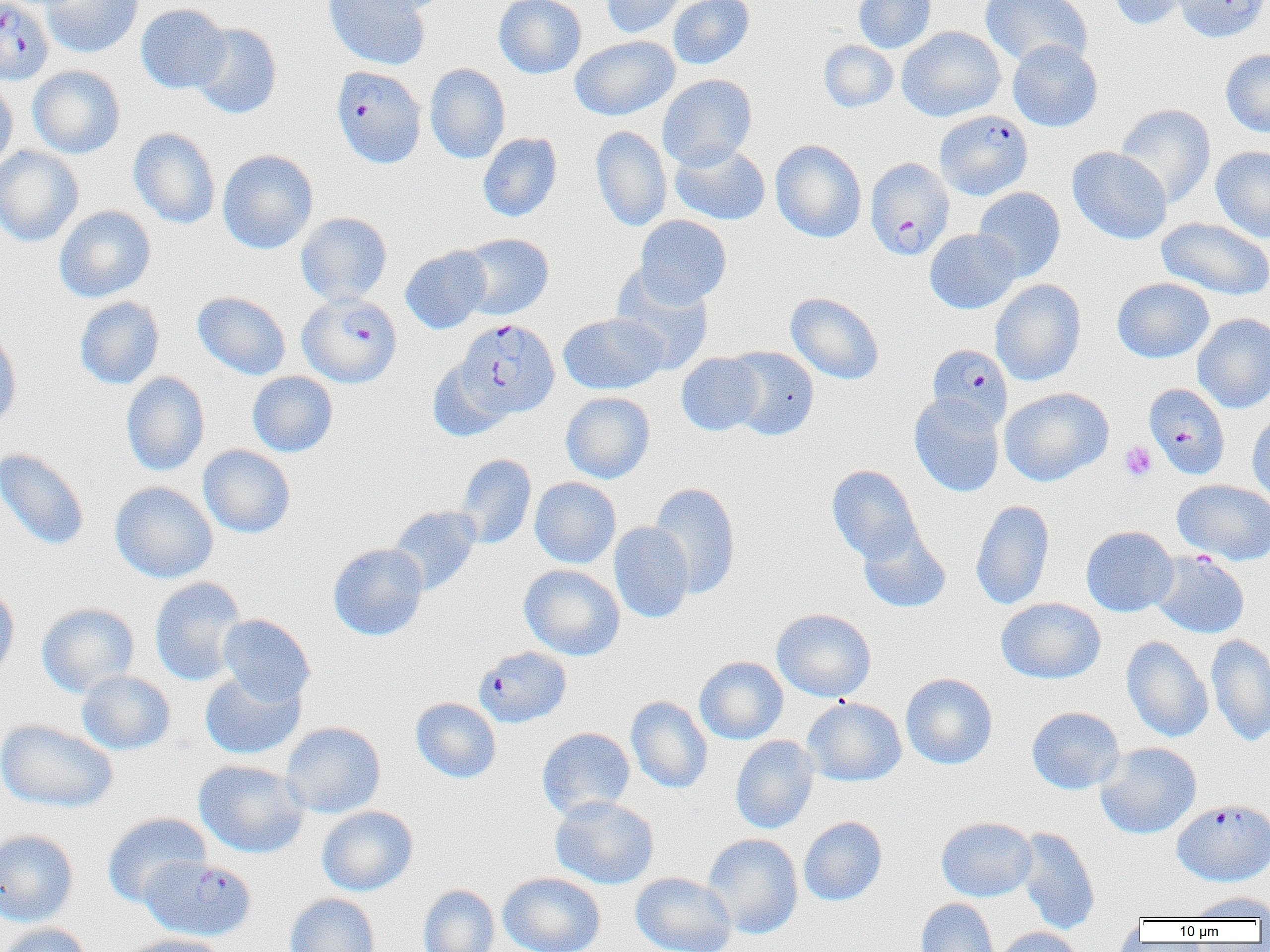
slide-level diagnosis = Plasmodium falciparum
image size = 1270×952 pixels
magnification = 1000x
platelet locations = approximate bounding boxes as [x1, y1, x2, y2] in pixels: [1119, 441, 1158, 481]
field of view = single
modality = light microscopy
Plasmodium falciparum-infected red blood cell locations = approximate bounding boxes as [x1, y1, x2, y2] in pixels: [0, 0, 53, 84], [331, 65, 427, 168], [934, 110, 1033, 200], [868, 157, 957, 259], [297, 293, 402, 387], [455, 318, 560, 419], [927, 343, 1013, 431], [1144, 383, 1230, 479], [474, 646, 572, 727], [1172, 799, 1270, 887], [139, 856, 257, 941]
preparation = thin blood smear
uninfected red blood cell locations = approximate bounding boxes as [x1, y1, x2, y2] in pixels: [41, 0, 143, 58], [323, 0, 431, 70], [354, 0, 453, 15], [493, 0, 586, 79], [600, 0, 689, 38], [668, 0, 754, 69], [853, 0, 936, 53], [979, 0, 1093, 69], [1107, 0, 1195, 30], [1172, 0, 1270, 42], [136, 4, 231, 93], [191, 22, 283, 119], [897, 26, 1006, 122], [570, 35, 679, 120], [818, 40, 898, 112], [1007, 40, 1103, 132], [1220, 49, 1270, 138], [425, 63, 510, 163], [27, 65, 126, 158], [657, 73, 757, 171], [0, 76, 18, 172], [1115, 104, 1216, 208], [590, 126, 672, 231], [128, 128, 221, 229], [478, 132, 562, 222], [770, 140, 867, 242], [670, 142, 771, 225], [1211, 145, 1270, 243], [0, 146, 84, 247], [1067, 146, 1172, 244], [218, 149, 318, 254], [973, 186, 1065, 281], [54, 205, 156, 302], [295, 212, 392, 304], [635, 215, 731, 308], [1156, 217, 1270, 301], [924, 228, 1022, 314], [457, 233, 554, 320], [400, 245, 492, 334], [610, 267, 716, 375], [1112, 277, 1214, 363], [990, 278, 1086, 386], [192, 291, 291, 380], [785, 291, 885, 385], [74, 296, 165, 389], [558, 312, 669, 395], [1192, 313, 1270, 413], [0, 328, 22, 432], [724, 346, 819, 440], [677, 352, 764, 435], [428, 360, 512, 442], [121, 371, 210, 476], [247, 371, 338, 457], [999, 387, 1114, 486], [561, 392, 655, 484], [909, 393, 1004, 496], [1247, 411, 1270, 508], [198, 445, 295, 538], [0, 447, 90, 551], [455, 453, 537, 548], [827, 464, 921, 564], [530, 477, 621, 568], [1173, 479, 1270, 565], [110, 481, 218, 583], [648, 482, 741, 599], [971, 499, 1056, 610], [388, 505, 481, 595], [608, 521, 694, 623], [858, 524, 951, 613], [1081, 526, 1179, 617], [328, 543, 428, 640], [1151, 551, 1250, 638], [519, 564, 625, 660], [149, 576, 248, 686], [0, 584, 20, 685], [996, 597, 1106, 684], [37, 602, 139, 696], [772, 608, 876, 702], [217, 613, 315, 706], [1206, 634, 1270, 746], [1121, 636, 1213, 742], [694, 656, 788, 745], [200, 669, 305, 760], [76, 670, 176, 755], [900, 672, 998, 769], [625, 696, 712, 793], [411, 697, 501, 783], [802, 697, 906, 786], [1026, 706, 1125, 794], [0, 719, 118, 813], [281, 721, 386, 818], [537, 726, 635, 819], [730, 735, 819, 834], [1095, 742, 1202, 839], [194, 760, 309, 858], [550, 796, 659, 889], [316, 805, 418, 896], [102, 812, 212, 907], [798, 816, 887, 906], [936, 817, 1037, 902], [1014, 827, 1101, 934], [0, 830, 79, 927], [702, 833, 803, 939], [498, 872, 606, 952], [631, 872, 737, 952], [417, 884, 500, 952], [1187, 890, 1270, 921], [284, 893, 381, 952], [915, 898, 1000, 952], [0, 922, 94, 952], [993, 926, 1084, 952], [121, 934, 228, 952]